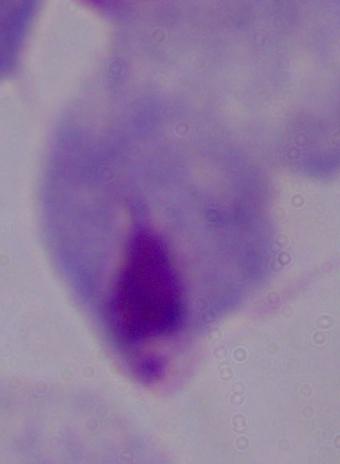

identification = trichomonad
magnification = 1000x
modality = photomicrograph